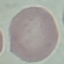

Summary:
  - Malaria status: uninfected
  - Image type: cell patch, automatically extracted from a larger field of view and resized to 64 × 64 pixels
  - Stain: Giemsa
  - Preparation: thin smear
  - Capture: smartphone through the microscope eyepiece